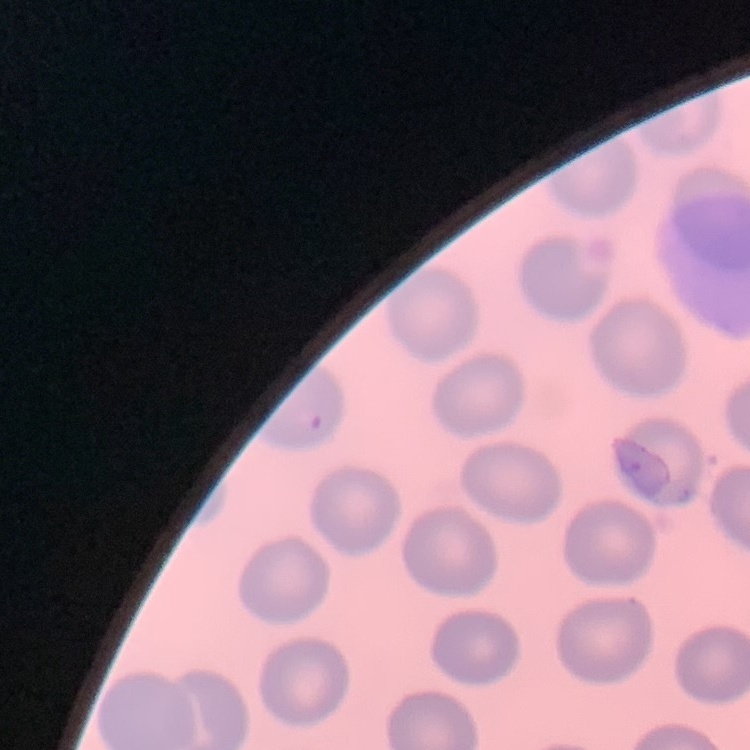
Summary:
  - Red blood cell morphology: no rouleaux formation
  - Image type: one tile cut from a larger photomicrograph
  - Stain: Field's or Giemsa
  - Preparation: thin blood film